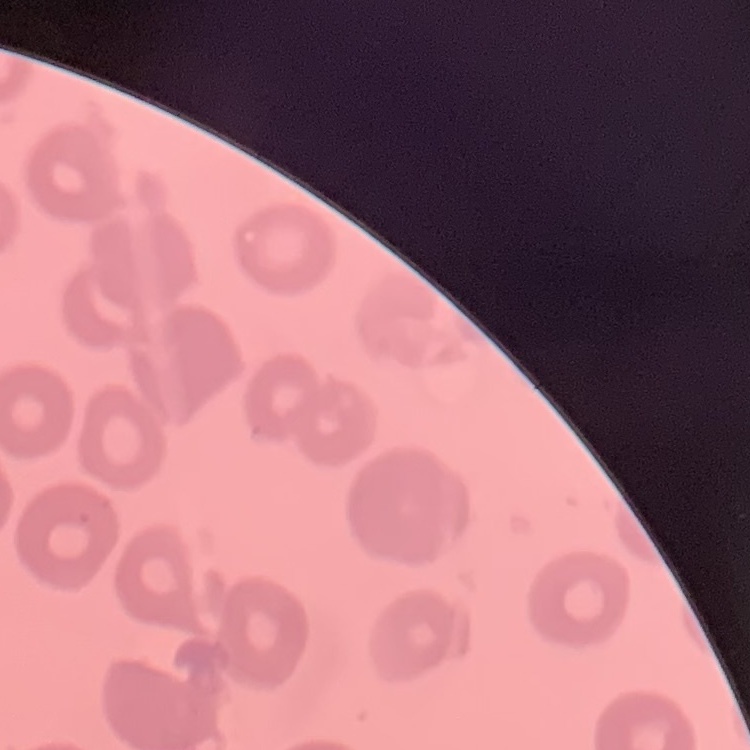
red blood cell morphology = no rouleaux formation
stain = Field's or Giemsa
image type = square crop of a larger photomicrograph
preparation = thin blood smear